Give a bounding box for every artifact (platelet-like body, stain precipitate, or debris).
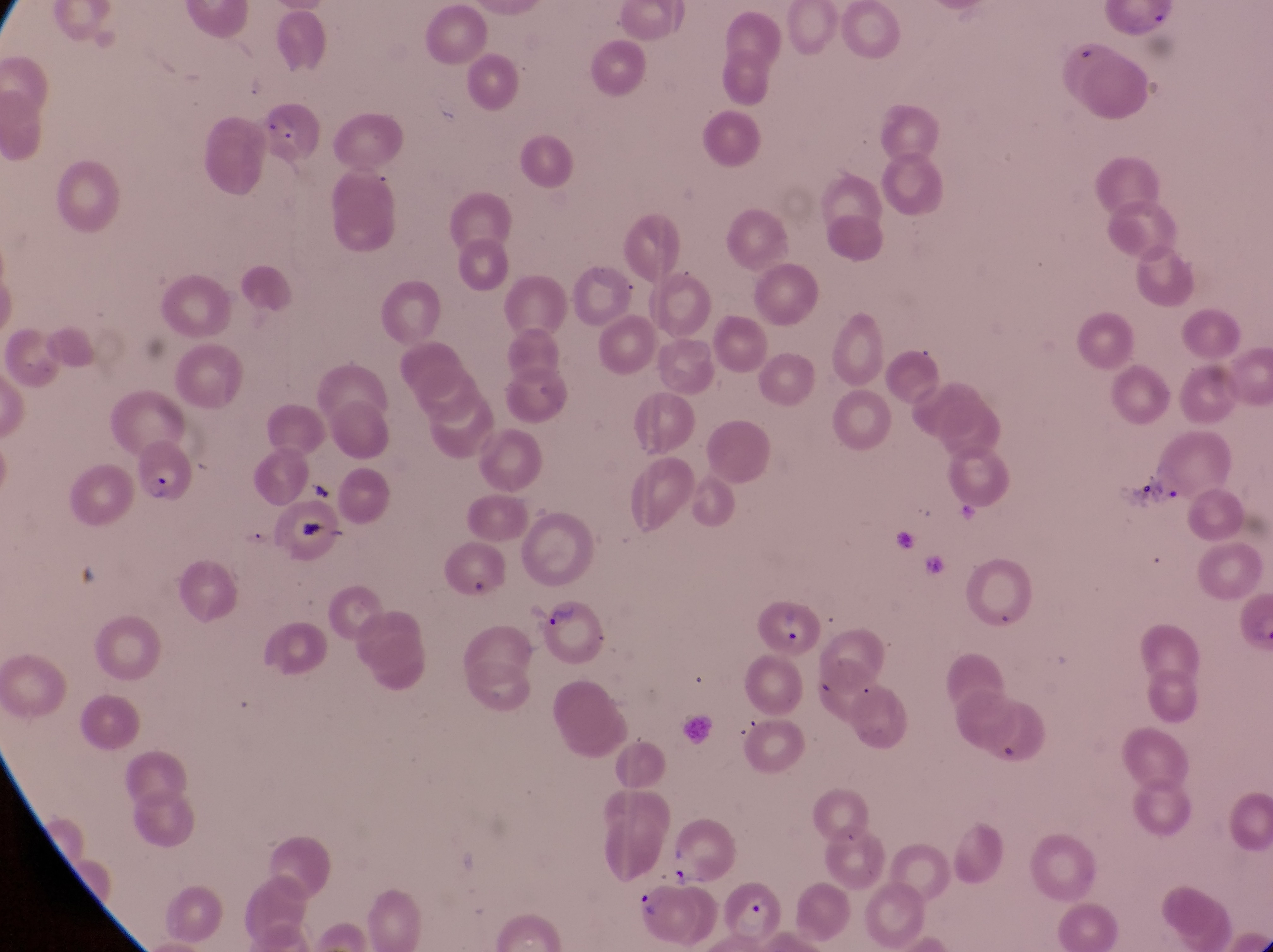
Approximate bounding boxes as left top right bottom in pixels.
Artifacts (platelet-like body, stain precipitate, or debris): 297 467 339 506; 289 507 324 546.

Summary:
  - Parasitised red blood cell locations: 135 437 195 514; 754 597 821 652; 529 599 607 667; 629 879 698 936; 722 879 791 949
  - Trophozoite locations: 1125 475 1158 512
  - Image size: 1273×952 pixels
  - Country: Uganda
  - Preparation: thin blood film
  - Field of view: single
  - Capture: smartphone photograph through the eyepiece of an Olympus CX-23 microscope
  - Magnification: 1000x